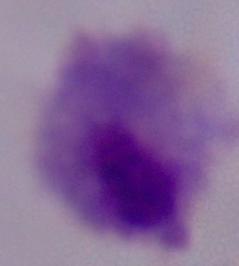

{
  "modality": "micrograph",
  "magnification": "1000x",
  "identification": "trichomonad"
}